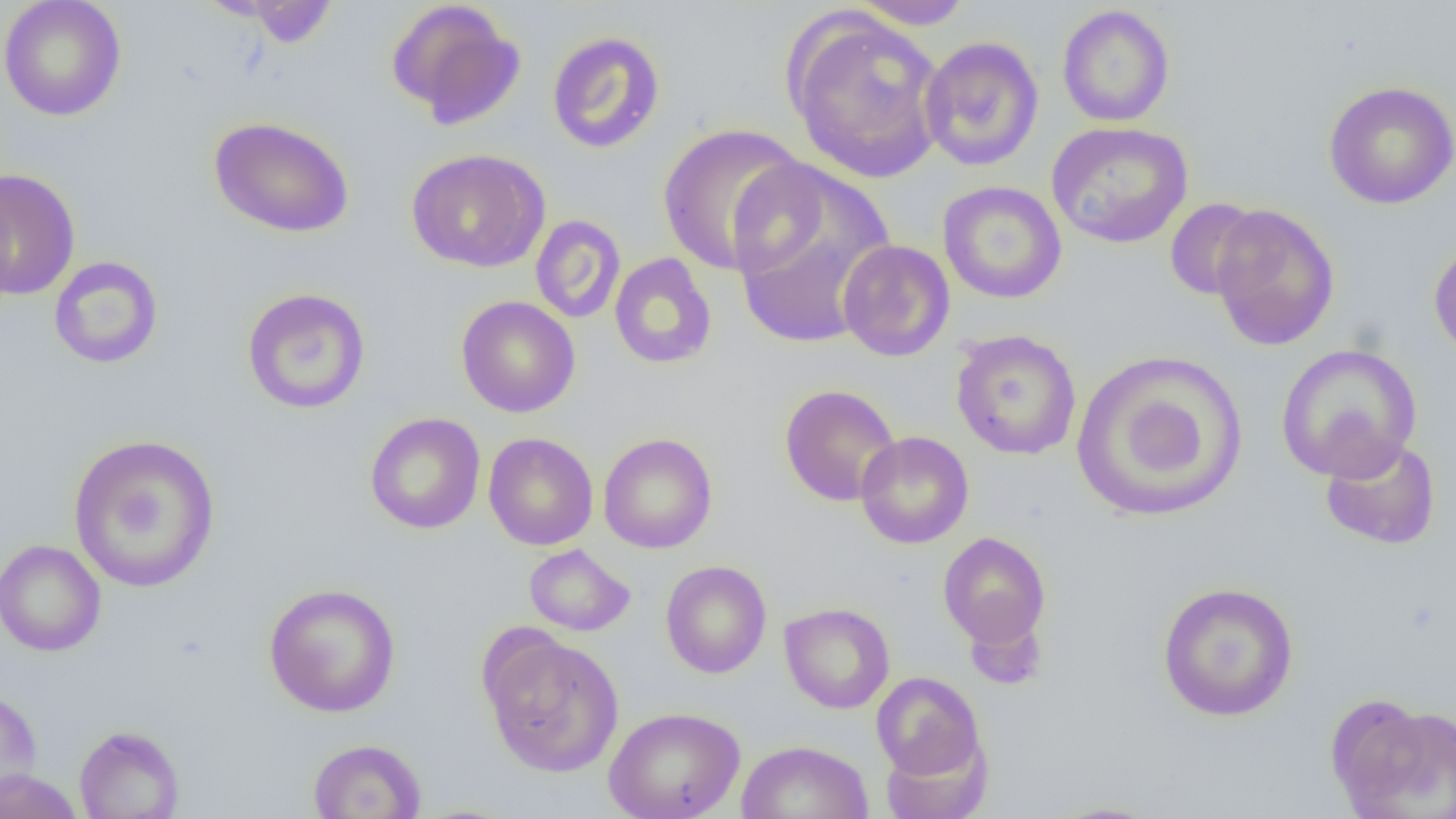

{
  "slide_level_diagnosis": "no evidence of blood parasites",
  "uninfected_red_blood_cell_locations": "approximate bounding boxes as (x1, y1, x2, y2) in pixels: (0, 0, 127, 121), (385, 0, 525, 130), (848, 0, 977, 30), (239, 1, 340, 48), (1057, 4, 1175, 127), (783, 9, 948, 184), (547, 31, 666, 154), (919, 36, 1045, 171), (1323, 81, 1456, 209), (209, 116, 354, 238), (1046, 121, 1193, 248), (657, 123, 811, 276), (406, 148, 549, 273), (728, 162, 898, 348), (0, 169, 80, 300), (937, 181, 1067, 304), (1164, 198, 1265, 301), (1209, 204, 1340, 351), (530, 215, 626, 324), (1428, 236, 1456, 362), (837, 239, 955, 362), (609, 252, 717, 370), (48, 256, 163, 369), (241, 287, 371, 414), (456, 296, 580, 417), (951, 329, 1082, 460), (1276, 343, 1422, 482), (1070, 351, 1246, 521), (779, 384, 901, 506), (365, 412, 486, 534), (855, 431, 974, 549), (483, 432, 598, 550), (598, 432, 718, 553), (67, 433, 221, 593), (1319, 434, 1441, 550), (938, 531, 1052, 649), (0, 539, 106, 657), (524, 544, 635, 636), (660, 560, 772, 679), (1156, 581, 1299, 722), (263, 583, 401, 718), (779, 602, 895, 714), (482, 631, 625, 777), (871, 672, 986, 781), (0, 688, 43, 801), (1332, 696, 1455, 818), (603, 706, 745, 819), (74, 725, 185, 819), (879, 728, 994, 819), (307, 738, 427, 819), (735, 740, 873, 819), (0, 769, 84, 819), (1046, 800, 1166, 819)",
  "preparation": "thin blood smear",
  "modality": "optical microscopy",
  "field_of_view": "one of a larger specimen",
  "magnification": "1000x",
  "image_size": "1456×819 pixels"
}